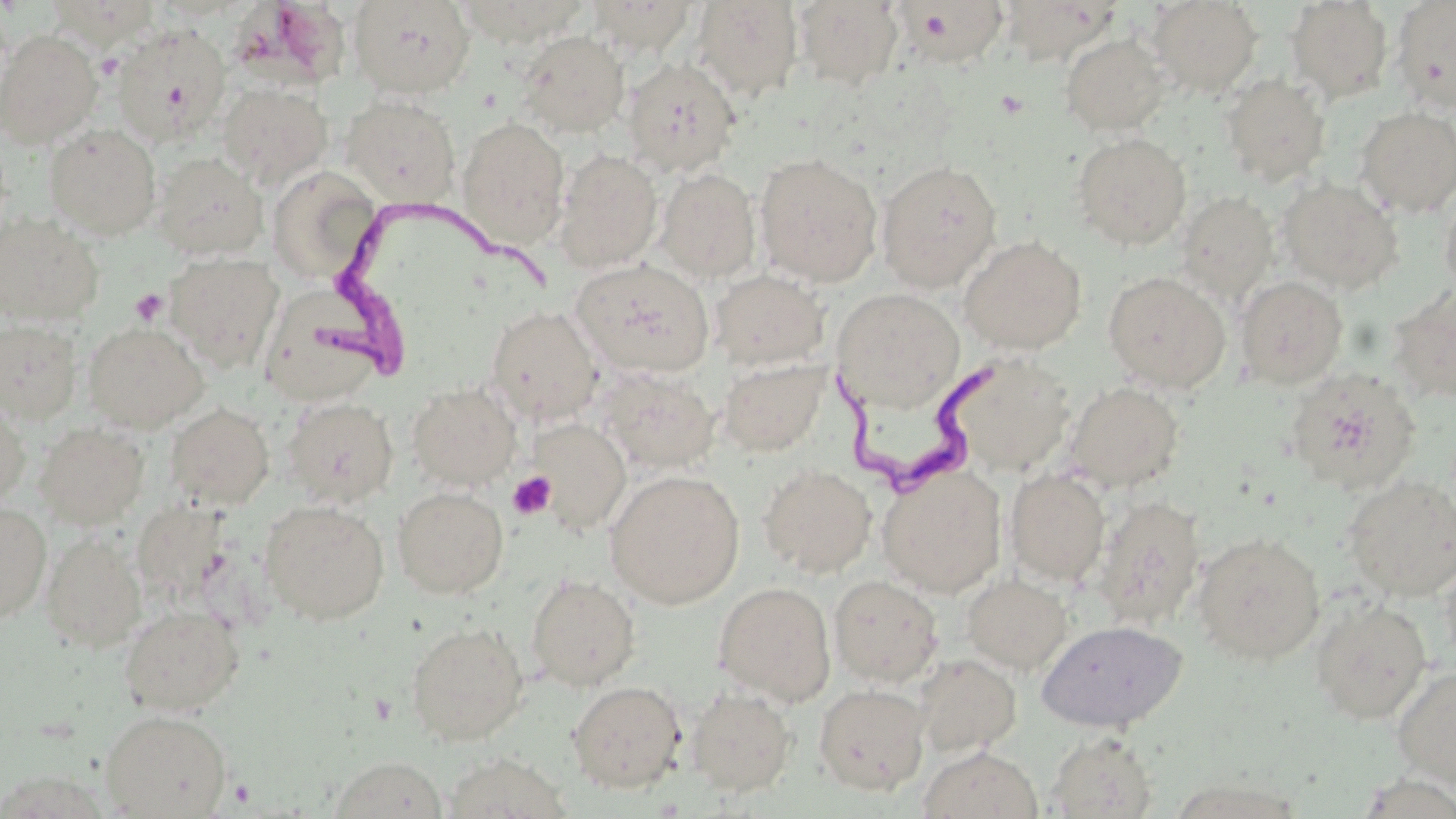

Approximate bounding boxes as (x1, y1, x2, y2) in pixels. Platelet locations: (95, 52, 124, 81), (996, 90, 1029, 118), (129, 288, 168, 327), (508, 471, 556, 520). Trypanosoma brucei locations: (316, 194, 555, 376), (826, 349, 1018, 506). Uninfected red blood cell locations: (349, 0, 476, 98), (588, 0, 697, 57), (1148, 0, 1262, 96), (1391, 0, 1456, 114), (49, 1, 160, 49), (456, 1, 588, 46), (692, 1, 804, 101), (793, 1, 904, 91), (1000, 1, 1108, 64), (1286, 1, 1393, 103), (903, 2, 1009, 69), (233, 3, 358, 93), (111, 23, 231, 146), (0, 30, 102, 148), (517, 31, 630, 138), (1060, 32, 1170, 136), (622, 56, 742, 177), (1220, 72, 1331, 186), (218, 83, 332, 189), (342, 95, 461, 206), (1356, 106, 1456, 216), (457, 116, 571, 250), (45, 124, 162, 239), (1072, 132, 1192, 250), (554, 148, 663, 272), (152, 152, 268, 261), (754, 152, 883, 287), (876, 160, 1002, 292), (268, 166, 379, 285), (656, 167, 761, 282), (1278, 178, 1403, 293), (1439, 188, 1456, 301), (1176, 190, 1278, 306), (0, 213, 104, 327), (959, 236, 1087, 355), (165, 252, 285, 370), (571, 258, 714, 378), (710, 269, 830, 371), (1103, 271, 1231, 394), (1235, 275, 1348, 389), (259, 282, 393, 406), (1389, 287, 1456, 404), (831, 288, 965, 412), (485, 305, 603, 424), (0, 319, 83, 424), (82, 322, 209, 432), (942, 352, 1077, 477), (718, 355, 830, 457), (1284, 366, 1423, 493), (596, 367, 720, 473), (1064, 381, 1184, 491), (408, 382, 520, 490), (0, 396, 31, 508), (282, 396, 399, 508), (165, 403, 275, 510), (528, 418, 631, 533), (34, 421, 149, 529), (759, 464, 877, 578), (877, 464, 1008, 597), (1005, 468, 1110, 586), (605, 469, 746, 609), (1342, 475, 1456, 601), (392, 486, 509, 599), (1093, 495, 1207, 629), (260, 500, 389, 625), (132, 501, 231, 603), (0, 502, 52, 624), (41, 531, 146, 652), (1191, 531, 1326, 664), (1439, 554, 1456, 671), (526, 573, 641, 691), (962, 573, 1072, 674), (828, 575, 944, 687), (713, 581, 836, 705), (1311, 598, 1432, 724), (119, 603, 244, 716), (1036, 620, 1187, 732), (406, 622, 529, 745), (913, 654, 1021, 758), (1392, 666, 1456, 788), (567, 680, 686, 794), (813, 683, 930, 795), (686, 687, 797, 797), (99, 709, 231, 818), (1045, 730, 1159, 818), (918, 745, 1043, 819), (442, 754, 572, 818), (328, 757, 450, 818). Slide-level diagnosis: Trypanosoma brucei. Image is 1456×819 pixels. Thin blood smear. 1000x magnification. May-Grünwald-Giemsa stain. Optical microscopy. One field of a larger specimen.